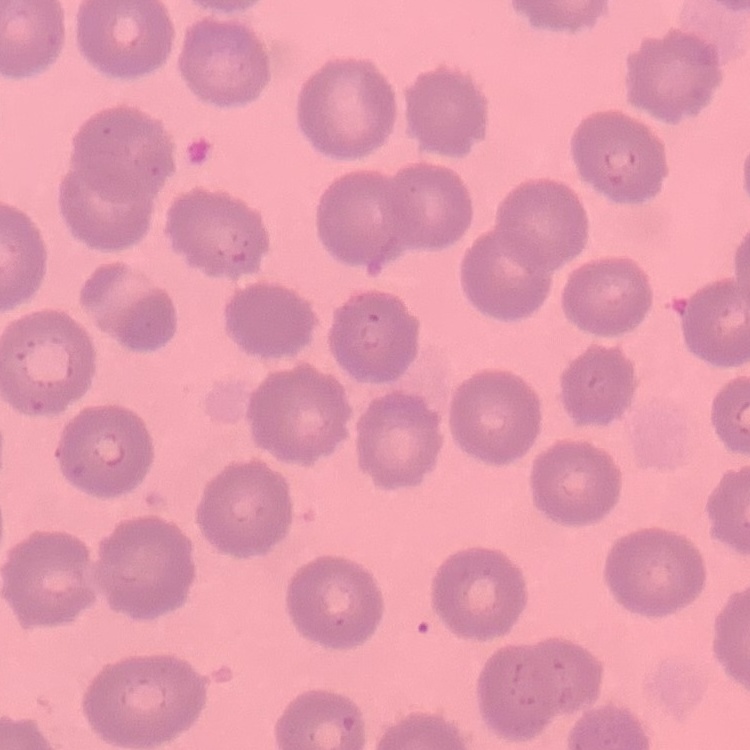
red_blood_cell_morphology: no rouleaux formation
image_type: square crop of a larger photomicrograph
preparation: thin blood smear
stain: Field's or Giemsa